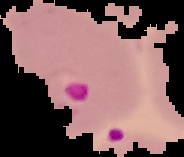

malaria status = parasitized
image size = 184×157 pixels
preparation = thin blood smear
image type = segmented cell region with the area outside set to black